Assess this cell for malaria.
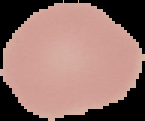

Uninfected.

preparation = thin blood film
image size = 145×121 pixels
image type = cell region segmented out of the field of view; surrounding area masked to black